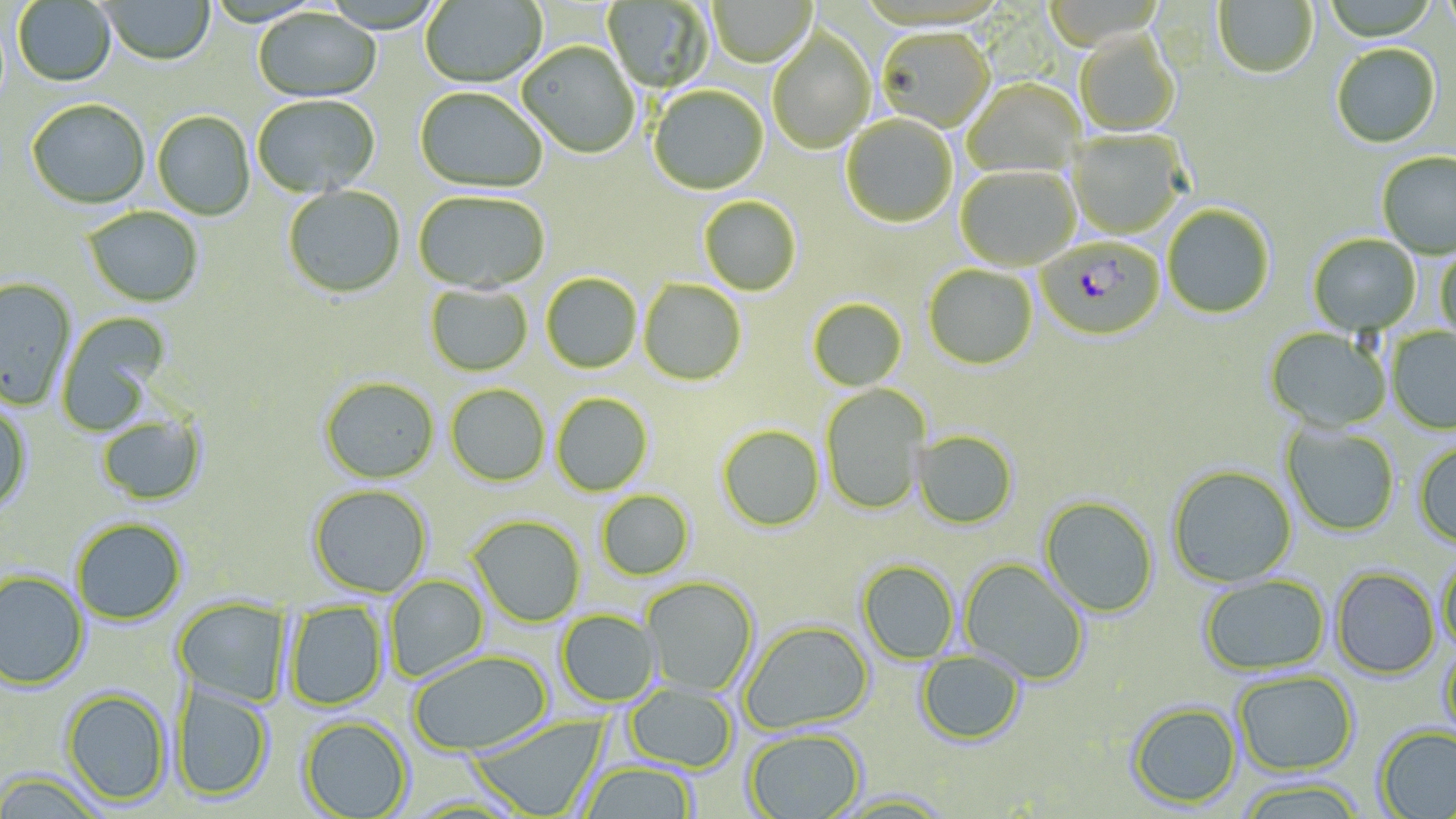
Summary:
  - Coordinate format: approximate bounding boxes as (x1,y1)-(x2,y2) corner pairs in pixels
  - Plasmodium falciparum-infected red blood cell locations: (1037,239)-(1165,341)
  - Uninfected red blood cell locations: (420,0)-(547,89), (1213,0)-(1318,80), (1321,0)-(1440,43), (12,1)-(117,88), (98,1)-(216,67), (602,1)-(715,94), (707,1)-(816,69), (253,8)-(381,104), (767,29)-(876,154), (876,30)-(996,134), (1074,34)-(1180,137), (517,42)-(641,159), (1331,46)-(1442,149), (961,80)-(1086,179), (648,86)-(769,196), (414,87)-(547,194), (252,95)-(381,199), (26,100)-(150,209), (152,112)-(255,220), (842,115)-(958,228), (1067,130)-(1188,240), (1377,152)-(1456,261), (955,166)-(1081,271), (283,185)-(405,299), (413,191)-(549,295), (699,197)-(801,296), (83,206)-(204,307), (1163,206)-(1274,319), (1308,235)-(1422,336), (1436,246)-(1456,343), (924,265)-(1038,371), (541,274)-(642,374), (0,278)-(76,409), (638,279)-(747,385), (425,284)-(533,377), (808,299)-(907,391), (57,312)-(172,435), (1386,327)-(1456,435), (1265,328)-(1392,433), (319,377)-(439,484), (446,384)-(550,487), (820,384)-(931,514), (551,393)-(653,496), (0,403)-(33,515), (96,414)-(208,506), (1280,423)-(1400,537), (717,425)-(825,532), (913,430)-(1018,529), (1412,441)-(1456,550), (1167,465)-(1298,588), (308,485)-(432,597), (597,491)-(694,581), (1039,496)-(1159,618), (468,515)-(586,627), (71,518)-(187,625), (1438,552)-(1456,656), (959,558)-(1089,686), (857,560)-(959,665), (1331,567)-(1440,679), (0,570)-(90,690), (384,575)-(490,684), (1199,575)-(1331,677), (640,576)-(758,697), (172,597)-(292,708), (284,601)-(389,711), (556,610)-(660,707), (739,620)-(874,735), (1438,642)-(1456,746), (408,650)-(551,756), (914,650)-(1027,746), (1232,671)-(1358,777), (171,682)-(274,803), (623,684)-(737,772), (60,688)-(172,806), (1127,702)-(1241,809), (469,713)-(610,818), (298,716)-(413,818), (1374,725)-(1456,819), (743,729)-(865,819), (579,761)-(698,818), (0,772)-(107,818), (1235,778)-(1368,819), (828,790)-(955,817)
  - Slide-level diagnosis: Plasmodium falciparum
  - Field of view: one of a larger specimen
  - Image size: 1456×819 pixels
  - Stain: May-Grünwald-Giemsa
  - Magnification: 1000x
  - Preparation: thin blood film
  - Modality: optical microscopy